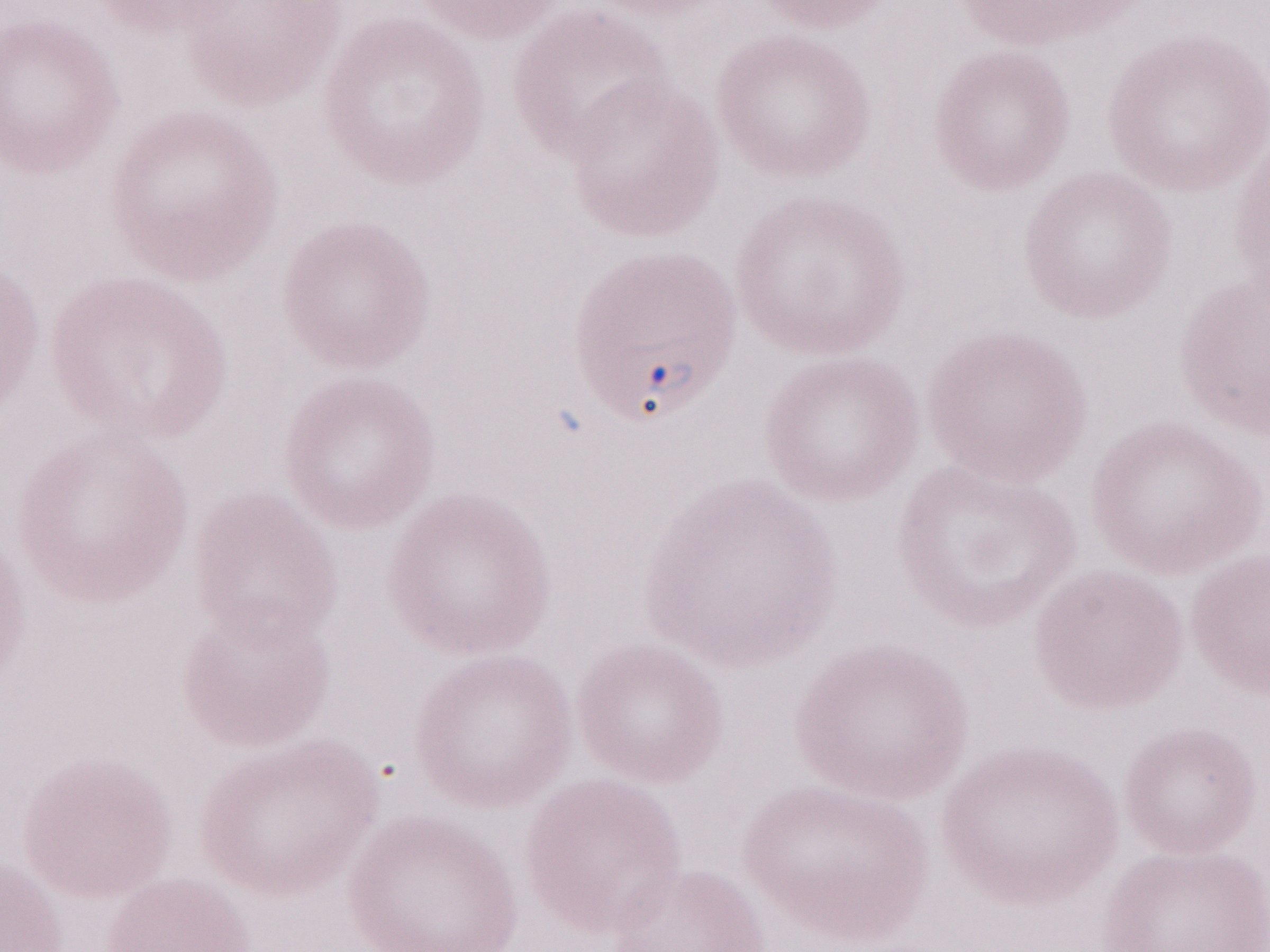 Image is 1270×952 pixels. May-Grünwald-Giemsa (MGG) stain. Patient diagnosis: malaria infection. One field of this slide. Olympus BX43 microscope, Olympus DP73 camera. Magnification: 1,000x. Thin peripheral-blood smear.